State the blood parasite species.
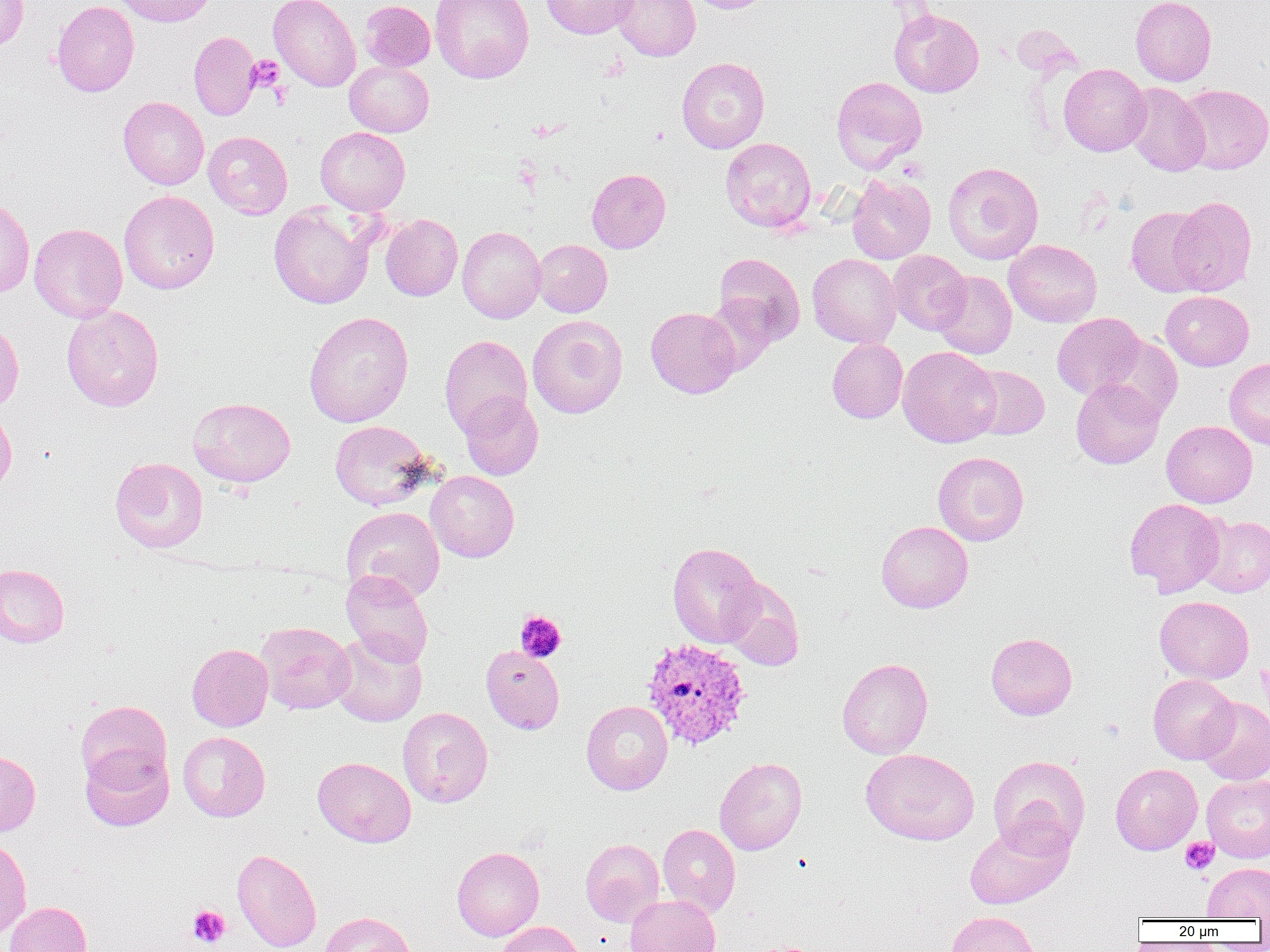
Plasmodium vivax.

Summary:
  - Coordinate format: approximate bounding boxes as named x1/y1/x2/y2 corners in pixels
  - Platelet locations: (x1=246, y1=55, x2=284, y2=92), (x1=515, y1=610, x2=566, y2=662), (x1=1180, y1=837, x2=1219, y2=875), (x1=188, y1=905, x2=230, y2=948)
  - Uninfected red blood cell locations: (x1=0, y1=0, x2=29, y2=51), (x1=115, y1=0, x2=218, y2=27), (x1=268, y1=0, x2=360, y2=92), (x1=430, y1=0, x2=534, y2=83), (x1=540, y1=0, x2=638, y2=39), (x1=611, y1=0, x2=700, y2=61), (x1=687, y1=0, x2=775, y2=13), (x1=1130, y1=0, x2=1216, y2=86), (x1=51, y1=1, x2=139, y2=96), (x1=358, y1=1, x2=436, y2=71), (x1=889, y1=8, x2=984, y2=97), (x1=188, y1=31, x2=260, y2=121), (x1=677, y1=57, x2=770, y2=153), (x1=344, y1=60, x2=434, y2=137), (x1=1058, y1=63, x2=1151, y2=156), (x1=831, y1=76, x2=927, y2=173), (x1=1123, y1=82, x2=1210, y2=177), (x1=1178, y1=84, x2=1270, y2=174), (x1=118, y1=97, x2=209, y2=189), (x1=315, y1=127, x2=410, y2=215), (x1=204, y1=131, x2=292, y2=218), (x1=720, y1=137, x2=816, y2=232), (x1=943, y1=162, x2=1044, y2=265), (x1=587, y1=169, x2=671, y2=253), (x1=847, y1=173, x2=936, y2=264), (x1=118, y1=190, x2=219, y2=294), (x1=1168, y1=195, x2=1256, y2=296), (x1=0, y1=197, x2=35, y2=297), (x1=269, y1=203, x2=376, y2=309), (x1=1126, y1=206, x2=1210, y2=296), (x1=380, y1=214, x2=463, y2=301), (x1=29, y1=223, x2=127, y2=323), (x1=457, y1=225, x2=545, y2=323), (x1=533, y1=239, x2=612, y2=317), (x1=1004, y1=239, x2=1102, y2=327), (x1=887, y1=250, x2=971, y2=334), (x1=714, y1=252, x2=805, y2=346), (x1=807, y1=253, x2=901, y2=348), (x1=932, y1=271, x2=1017, y2=359), (x1=1161, y1=291, x2=1253, y2=371), (x1=703, y1=295, x2=780, y2=373), (x1=61, y1=304, x2=164, y2=412), (x1=645, y1=307, x2=740, y2=398), (x1=303, y1=311, x2=414, y2=427), (x1=1052, y1=313, x2=1145, y2=399), (x1=527, y1=315, x2=628, y2=418), (x1=0, y1=321, x2=23, y2=413), (x1=440, y1=334, x2=532, y2=436), (x1=1099, y1=335, x2=1183, y2=423), (x1=827, y1=338, x2=907, y2=423), (x1=898, y1=346, x2=1001, y2=447), (x1=1224, y1=358, x2=1270, y2=450), (x1=968, y1=365, x2=1049, y2=439), (x1=1071, y1=378, x2=1164, y2=469), (x1=459, y1=391, x2=543, y2=480), (x1=188, y1=397, x2=296, y2=487), (x1=0, y1=407, x2=17, y2=496), (x1=329, y1=420, x2=435, y2=510), (x1=1161, y1=421, x2=1257, y2=508), (x1=933, y1=451, x2=1029, y2=546), (x1=110, y1=457, x2=208, y2=553), (x1=426, y1=471, x2=519, y2=562), (x1=1123, y1=498, x2=1226, y2=597), (x1=341, y1=506, x2=445, y2=602), (x1=1196, y1=514, x2=1270, y2=597), (x1=876, y1=520, x2=973, y2=613), (x1=667, y1=542, x2=764, y2=648), (x1=0, y1=563, x2=70, y2=647), (x1=341, y1=569, x2=433, y2=667), (x1=720, y1=577, x2=805, y2=671), (x1=1155, y1=596, x2=1254, y2=683), (x1=256, y1=622, x2=356, y2=714), (x1=329, y1=632, x2=427, y2=727), (x1=986, y1=632, x2=1077, y2=720), (x1=187, y1=643, x2=273, y2=731), (x1=480, y1=645, x2=565, y2=734), (x1=837, y1=657, x2=933, y2=759), (x1=1147, y1=674, x2=1239, y2=764), (x1=1196, y1=697, x2=1270, y2=785), (x1=75, y1=700, x2=172, y2=790), (x1=581, y1=700, x2=673, y2=795), (x1=398, y1=707, x2=492, y2=808), (x1=178, y1=731, x2=270, y2=822), (x1=80, y1=745, x2=174, y2=832), (x1=860, y1=748, x2=979, y2=845), (x1=0, y1=750, x2=41, y2=837), (x1=988, y1=755, x2=1090, y2=858), (x1=313, y1=757, x2=416, y2=847), (x1=714, y1=757, x2=807, y2=855), (x1=1111, y1=763, x2=1202, y2=855), (x1=1202, y1=774, x2=1270, y2=863), (x1=964, y1=819, x2=1073, y2=910), (x1=658, y1=824, x2=740, y2=917), (x1=0, y1=836, x2=31, y2=941), (x1=580, y1=838, x2=664, y2=927), (x1=452, y1=846, x2=544, y2=941), (x1=232, y1=848, x2=322, y2=952), (x1=1202, y1=861, x2=1270, y2=920), (x1=624, y1=895, x2=720, y2=952), (x1=5, y1=901, x2=92, y2=952), (x1=946, y1=911, x2=1041, y2=952), (x1=320, y1=912, x2=416, y2=952), (x1=496, y1=921, x2=585, y2=952)
  - Plasmodium vivax-infected red blood cell locations: (x1=640, y1=637, x2=753, y2=751)
  - Image size: 1270×952 pixels
  - Preparation: thin blood smear
  - Magnification: 1000x
  - Modality: optical microscopy
  - Field of view: one of a larger specimen